Locate every blood parasite and identify its species.
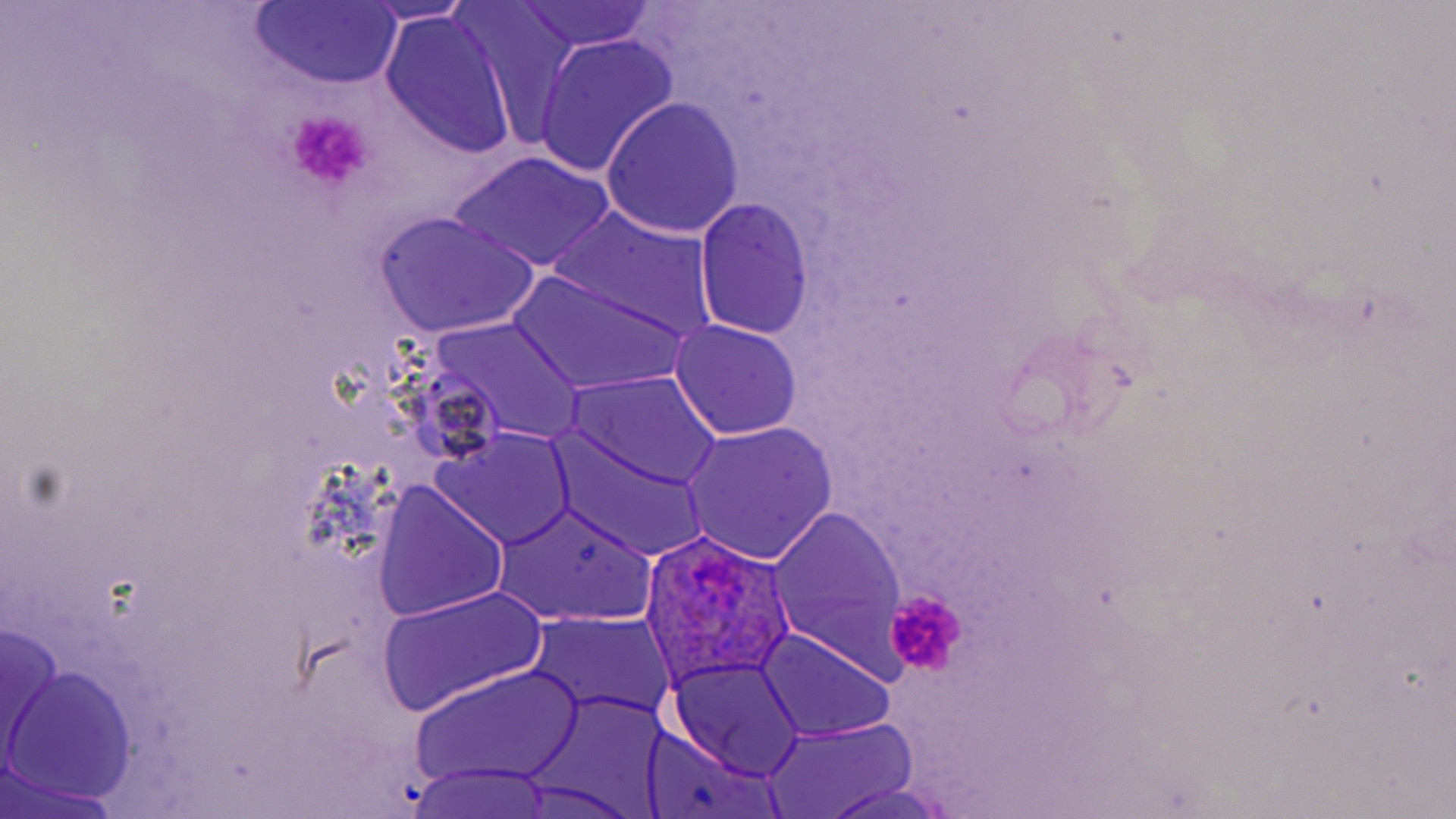
Approximate bounding boxes as named x1/y1/x2/y2 corners in pixels.
Plasmodium ovale-infected red blood cells: (x1=639, y1=532, x2=800, y2=688).
No Plasmodium falciparum, Plasmodium malariae, Plasmodium vivax, Babesia divergens, or Trypanosoma brucei observed.

Summary:
  - Uninfected red blood cell locations: (x1=358, y1=1, x2=477, y2=24), (x1=452, y1=2, x2=586, y2=146), (x1=514, y1=2, x2=657, y2=53), (x1=249, y1=3, x2=401, y2=86), (x1=379, y1=12, x2=519, y2=161), (x1=531, y1=33, x2=679, y2=178), (x1=601, y1=96, x2=743, y2=237), (x1=448, y1=151, x2=616, y2=274), (x1=694, y1=198, x2=814, y2=338), (x1=546, y1=206, x2=718, y2=344), (x1=373, y1=211, x2=539, y2=340), (x1=510, y1=272, x2=688, y2=394), (x1=430, y1=318, x2=585, y2=444), (x1=671, y1=320, x2=803, y2=439), (x1=571, y1=372, x2=722, y2=489), (x1=681, y1=421, x2=840, y2=564), (x1=431, y1=430, x2=576, y2=551), (x1=547, y1=430, x2=710, y2=559), (x1=371, y1=483, x2=509, y2=621), (x1=494, y1=501, x2=656, y2=626), (x1=767, y1=506, x2=911, y2=675), (x1=377, y1=585, x2=549, y2=716), (x1=523, y1=613, x2=676, y2=728), (x1=2, y1=620, x2=64, y2=768), (x1=756, y1=630, x2=895, y2=743), (x1=667, y1=659, x2=806, y2=783), (x1=411, y1=664, x2=585, y2=788), (x1=5, y1=667, x2=140, y2=804), (x1=532, y1=691, x2=674, y2=808), (x1=761, y1=718, x2=921, y2=817), (x1=645, y1=731, x2=784, y2=819), (x1=405, y1=765, x2=561, y2=819), (x1=0, y1=772, x2=127, y2=818), (x1=507, y1=779, x2=644, y2=817), (x1=818, y1=783, x2=959, y2=819)
  - Platelet locations: (x1=287, y1=109, x2=374, y2=191), (x1=884, y1=589, x2=967, y2=676)
  - Slide-level diagnosis: Plasmodium ovale
  - Stain: May-Grünwald-Giemsa
  - Preparation: thin blood smear
  - Modality: optical microscopy
  - Image size: 1456×819 pixels
  - Magnification: 1000x
  - Field of view: single